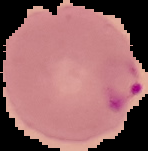

{
  "image_type": "segmented cell region on a black background",
  "preparation": "thin blood film",
  "image_size": "148×151 pixels",
  "malaria_status": "parasitized"
}